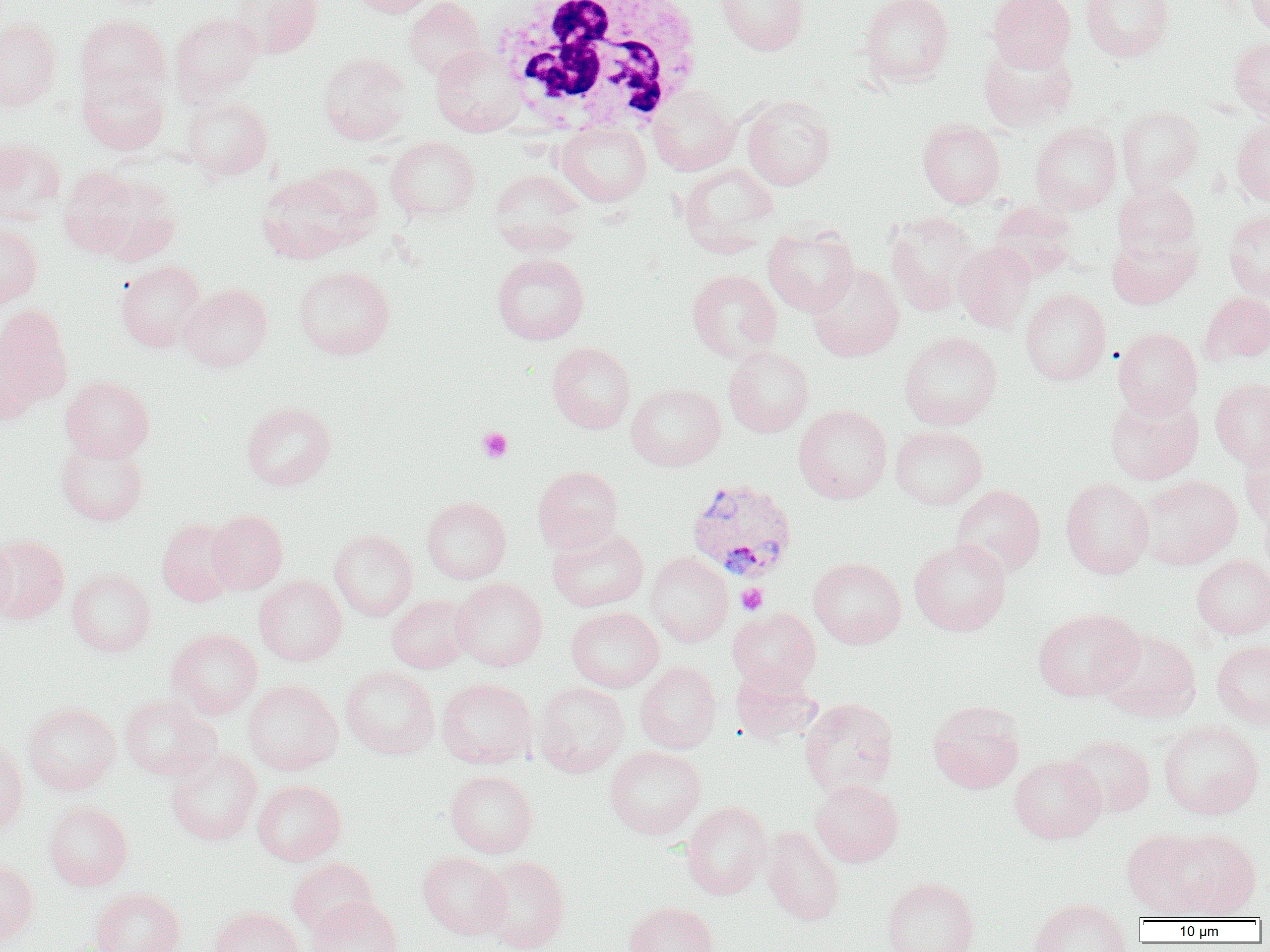

{
  "slide_level_diagnosis": "Plasmodium vivax",
  "field_of_view": "one of a larger specimen",
  "white_blood_cell_locations": "approximate bounding boxes as [x1, y1, x2, y2] in pixels: [489, 0, 705, 135]",
  "image_size": "1270×952 pixels",
  "plasmodium_vivax_infected_red_blood_cell_locations": "approximate bounding boxes as [x1, y1, x2, y2] in pixels: [686, 477, 798, 582]",
  "platelet_locations": "approximate bounding boxes as [x1, y1, x2, y2] in pixels: [478, 427, 512, 462], [735, 584, 768, 615]",
  "preparation": "thin blood smear",
  "uninfected_red_blood_cell_locations": "approximate bounding boxes as [x1, y1, x2, y2] in pixels: [230, 0, 323, 58], [348, 0, 438, 17], [404, 0, 487, 81], [714, 0, 810, 56], [858, 0, 955, 87], [988, 0, 1075, 71], [1080, 0, 1174, 61], [1246, 0, 1270, 37], [170, 11, 264, 103], [75, 14, 170, 100], [0, 17, 62, 111], [1229, 37, 1270, 121], [978, 40, 1078, 132], [431, 44, 526, 136], [316, 52, 412, 145], [77, 72, 168, 155], [647, 85, 741, 176], [741, 94, 836, 191], [182, 97, 273, 180], [1116, 105, 1205, 193], [917, 118, 1006, 207], [1232, 118, 1270, 206], [555, 121, 651, 206], [1030, 121, 1122, 214], [385, 136, 480, 222], [0, 138, 65, 224], [678, 163, 779, 255], [60, 166, 180, 263], [489, 169, 587, 256], [255, 171, 370, 264], [1112, 179, 1200, 261], [988, 201, 1079, 283], [1224, 210, 1270, 301], [884, 211, 982, 316], [0, 221, 43, 308], [763, 225, 860, 316], [1107, 232, 1200, 309], [954, 241, 1037, 333], [491, 253, 590, 345], [116, 260, 206, 352], [808, 264, 905, 362], [294, 265, 395, 360], [687, 270, 782, 363], [179, 283, 273, 372], [1020, 289, 1111, 385], [1199, 292, 1270, 366], [1, 304, 74, 405], [1113, 327, 1202, 420], [899, 331, 1002, 430], [0, 342, 40, 425], [547, 342, 636, 433], [723, 346, 814, 437], [60, 375, 154, 462], [1210, 378, 1270, 469], [626, 383, 726, 471], [1105, 392, 1204, 485], [241, 401, 336, 490], [794, 404, 892, 503], [890, 426, 987, 510], [1240, 436, 1270, 530], [56, 437, 149, 526], [533, 466, 623, 554], [1138, 475, 1243, 569], [1060, 477, 1154, 579], [950, 485, 1046, 578], [1258, 492, 1270, 577], [422, 496, 511, 584], [207, 509, 288, 594], [157, 518, 240, 606], [546, 527, 649, 612], [329, 529, 418, 620], [0, 534, 70, 624], [0, 537, 16, 623], [909, 538, 1011, 636], [646, 552, 733, 647], [1192, 555, 1270, 638], [808, 557, 906, 648], [67, 567, 156, 657], [254, 575, 347, 665], [452, 578, 548, 671], [387, 594, 474, 673], [566, 607, 664, 692], [727, 607, 821, 692], [1032, 608, 1144, 701], [167, 629, 263, 719], [1098, 629, 1201, 723], [1211, 640, 1270, 729], [635, 661, 722, 754], [341, 665, 439, 759], [731, 666, 822, 744], [437, 678, 537, 768], [242, 679, 343, 775], [533, 682, 630, 777], [120, 694, 221, 780], [799, 697, 899, 797], [928, 700, 1025, 793], [23, 702, 121, 795], [37, 702, 126, 891], [1158, 720, 1264, 819], [1063, 734, 1156, 818], [0, 740, 28, 834], [604, 745, 706, 839], [165, 748, 263, 846], [1009, 755, 1105, 843], [445, 770, 538, 858], [810, 779, 903, 866], [252, 780, 346, 866], [43, 800, 133, 891], [681, 800, 771, 900], [761, 826, 844, 926], [1122, 828, 1216, 918], [1167, 828, 1260, 919], [418, 851, 510, 939], [479, 856, 570, 952], [287, 858, 378, 936], [0, 859, 39, 945], [881, 877, 979, 952], [90, 888, 185, 952], [307, 897, 401, 952], [1029, 898, 1133, 952], [624, 901, 718, 952], [209, 906, 304, 952]",
  "magnification": "1000x",
  "modality": "light microscopy"
}